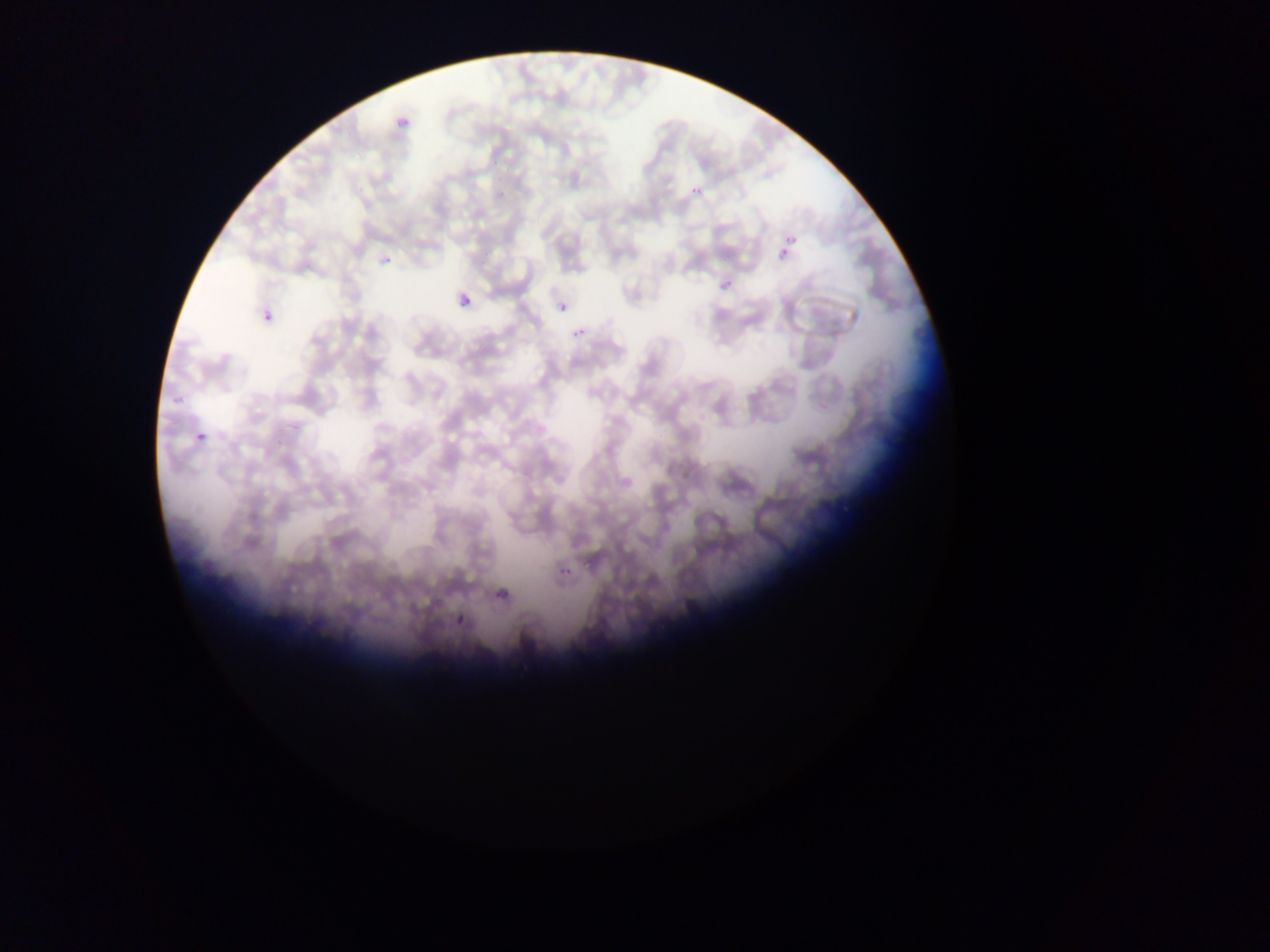

Approximate bounding boxes as [left, top, right, bottom] in pixels.
Summary:
  - Malaria parasite locations: [391, 113, 421, 132], [685, 179, 705, 196], [781, 234, 801, 253], [779, 247, 789, 258], [374, 252, 395, 272], [709, 273, 738, 295], [454, 293, 473, 313], [559, 301, 569, 312], [261, 309, 282, 322], [573, 327, 585, 337], [173, 392, 190, 415], [195, 431, 207, 443], [556, 555, 573, 578], [494, 573, 531, 600], [456, 614, 467, 626]
  - Image size: 1270×952 pixels
  - Preparation: thin blood smear
  - Field of view: single
  - Country: Ghana
  - Capture: mobile-phone photograph through a microscope